Name the parasite shown.
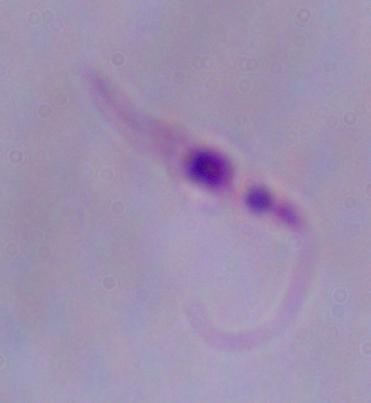

Leishmania.

Summary:
  - Modality: photomicrograph
  - Magnification: 1000x